Assess this cell for malaria.
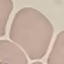
It is uninfected.

preparation = thin smear
image type = cell patch, automatically extracted from a larger field of view and resized to 64 × 64 pixels
capture = smartphone camera at the microscope eyepiece
stain = Giemsa